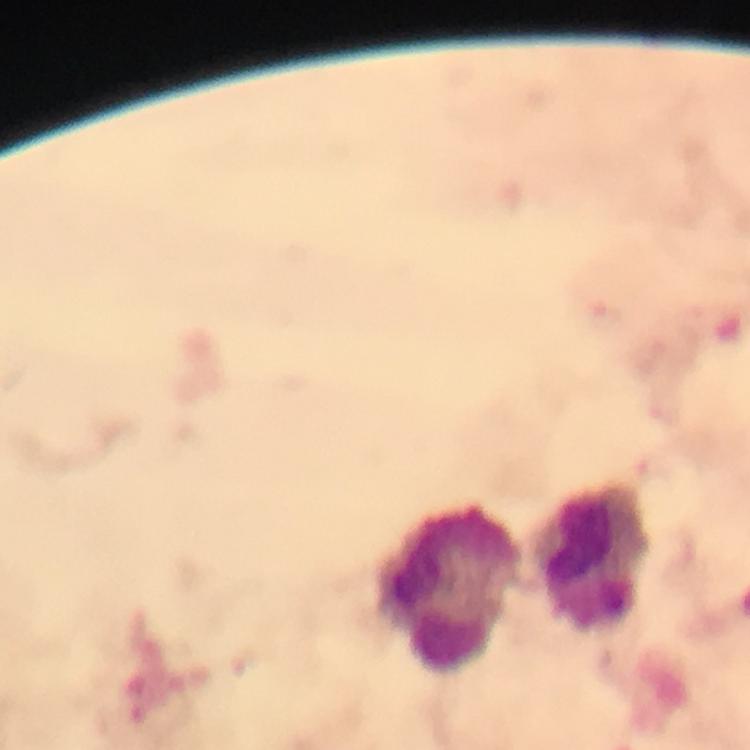

Approximate centers as {x, y} in pixels.
Summary:
  - Leukocyte locations: {594, 561}, {451, 592}
  - Capture: smartphone mounted on the microscope
  - Stain: Giemsa
  - Context: from a malaria diagnostic workup
  - Cropped from: a single field of view
  - Preparation: thick blood film
  - Image size: 750×750 pixels
  - Magnification: 100x
  - Immersion oil: applied
  - Malaria parasites: none seen